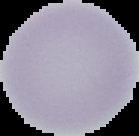

The area outside the segmented cell region is set to black. From a thin blood film. Malaria status: uninfected. Image is 139×136 pixels.